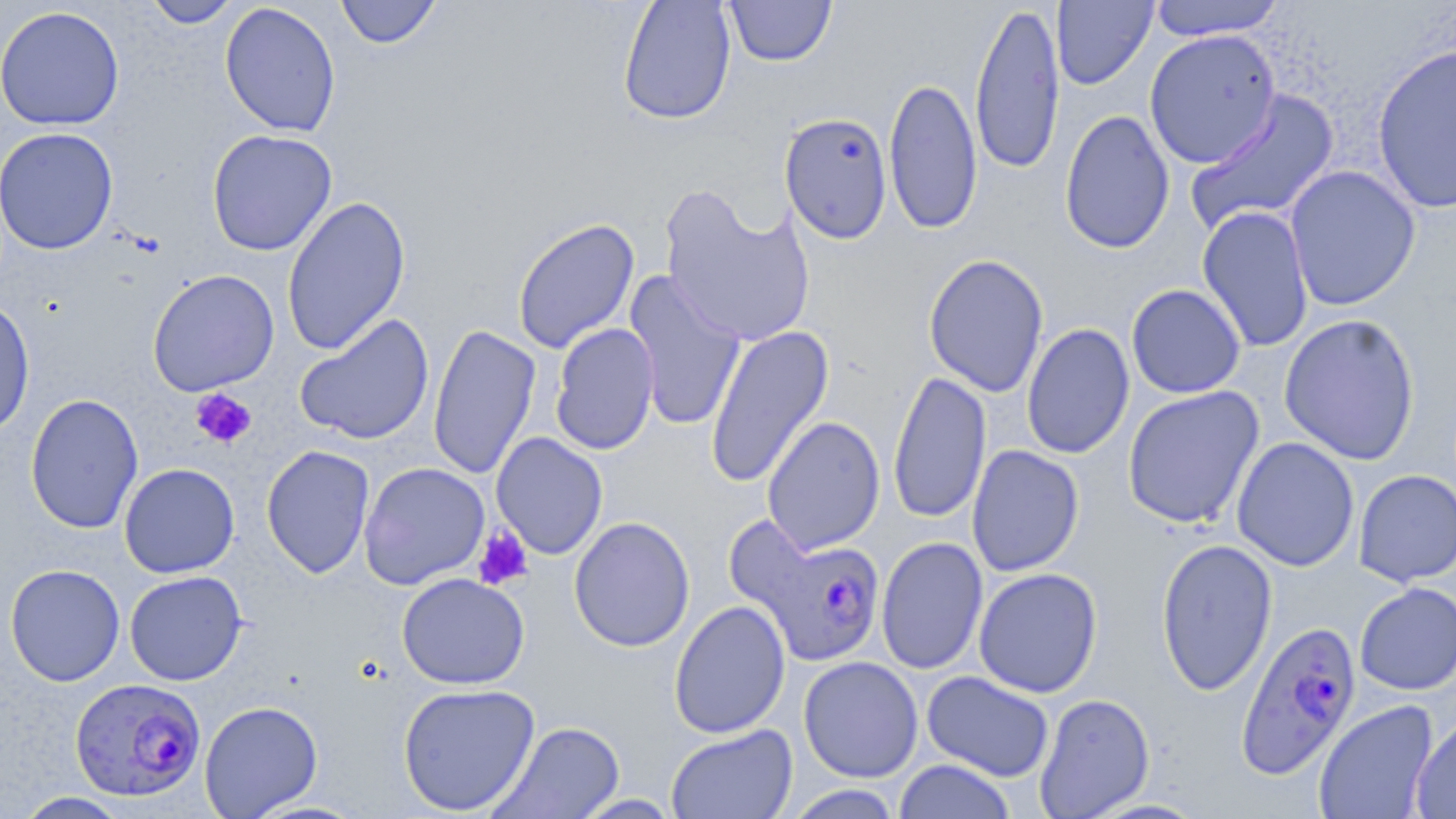 Approximate bounding boxes as (x1,y1)-(x2,y2) corner pairs in pixels. Plasmodium falciparum-infected red blood cell locations: (726,512)-(885,667), (1234,619)-(1362,779), (69,677)-(207,802). Platelet locations: (190,387)-(257,450), (472,526)-(533,591). Uninfected red blood cell locations: (143,0)-(244,28), (335,0)-(442,49), (618,0)-(736,125), (724,0)-(837,67), (1052,0)-(1158,90), (1147,0)-(1287,41), (970,1)-(1066,176), (219,2)-(341,138), (0,4)-(125,131), (1143,29)-(1281,169), (1371,42)-(1455,215), (883,77)-(983,235), (1185,88)-(1340,234), (1059,109)-(1175,254), (779,112)-(893,244), (0,127)-(118,255), (207,129)-(337,256), (1284,165)-(1421,311), (660,187)-(816,348), (282,195)-(411,356), (1196,205)-(1314,353), (512,217)-(640,354), (923,253)-(1050,398), (147,269)-(280,396), (623,271)-(746,432), (1126,283)-(1246,399), (0,297)-(35,439), (294,313)-(434,446), (1278,313)-(1421,465), (549,322)-(660,456), (427,323)-(541,480), (1021,323)-(1135,460), (705,324)-(835,488), (888,369)-(991,525), (1122,386)-(1265,529), (25,393)-(144,534), (762,416)-(886,554), (491,432)-(608,560), (1232,437)-(1360,572), (261,445)-(376,578), (966,445)-(1085,577), (358,461)-(490,590), (119,463)-(239,578), (1354,469)-(1456,587), (568,516)-(695,653), (876,536)-(988,675), (1155,537)-(1278,696), (5,564)-(125,687), (973,567)-(1103,698), (124,570)-(247,686), (396,572)-(530,690), (1354,582)-(1456,695), (669,600)-(791,738), (798,656)-(923,782), (921,671)-(1055,782), (397,682)-(541,816), (1034,693)-(1155,818), (199,700)-(323,818), (1313,700)-(1439,819), (1411,714)-(1456,819), (489,720)-(625,818), (665,724)-(798,819), (894,760)-(1016,819), (783,785)-(908,818), (14,792)-(134,818), (571,794)-(681,818). Slide-level diagnosis: Plasmodium falciparum. May-Grünwald-Giemsa-stained preparation. Thin blood smear. 1000x magnification. Image is 1456×819 pixels. Optical microscopy. One field of a larger specimen.